Name the cell type shown.
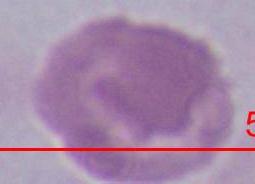

This is an erythrocyte.

Photomicrograph. Captured at 1000x magnification.